State the preparation type.
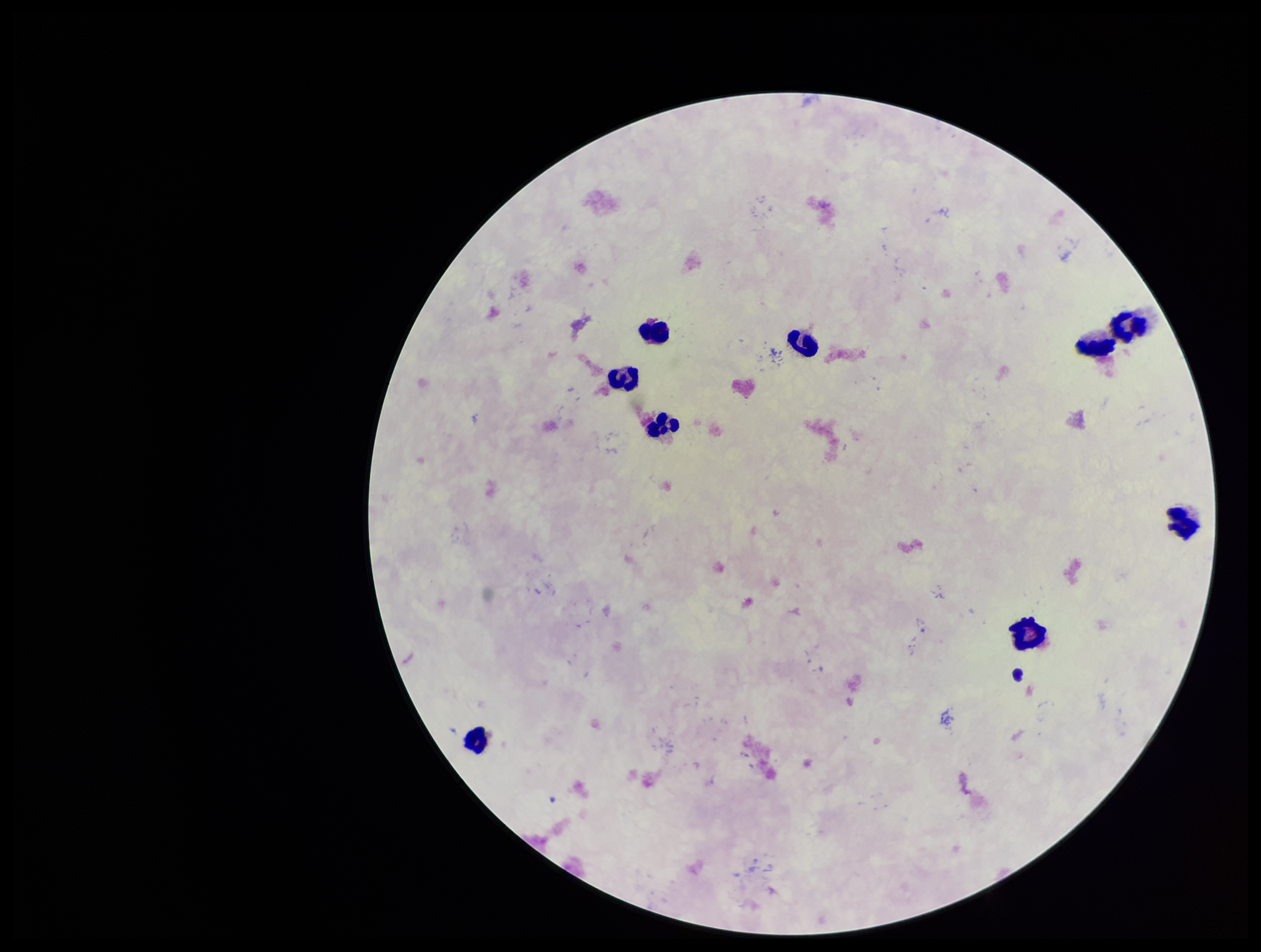
A thick smear.

field of view = single
capture = smartphone photograph through the microscope eyepiece
leukocyte count = 9
image size = 1261×952 pixels
parasite count = 0
patient malaria status = negative
stain = Giemsa
Plasmodium parasites = none seen